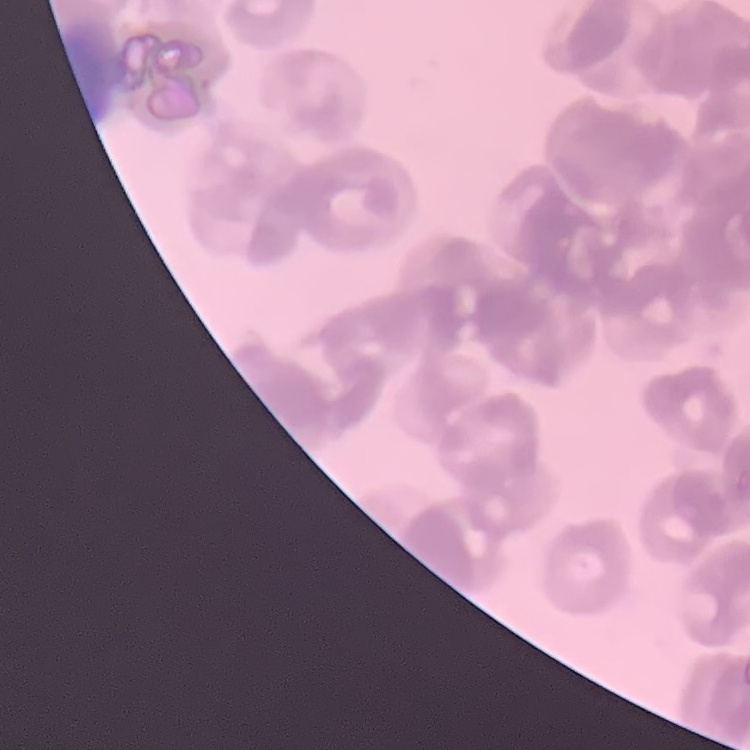
Summary:
  - Red blood cell morphology: rouleaux formation
  - Preparation: thin blood film
  - Stain: Field's or Giemsa
  - Image type: square crop of a larger photomicrograph